Classify this cell by malaria status.
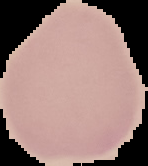

Uninfected.

{
  "preparation": "thin blood smear",
  "image_size": "148×166 pixels",
  "image_type": "segmented cell region on a black background"
}